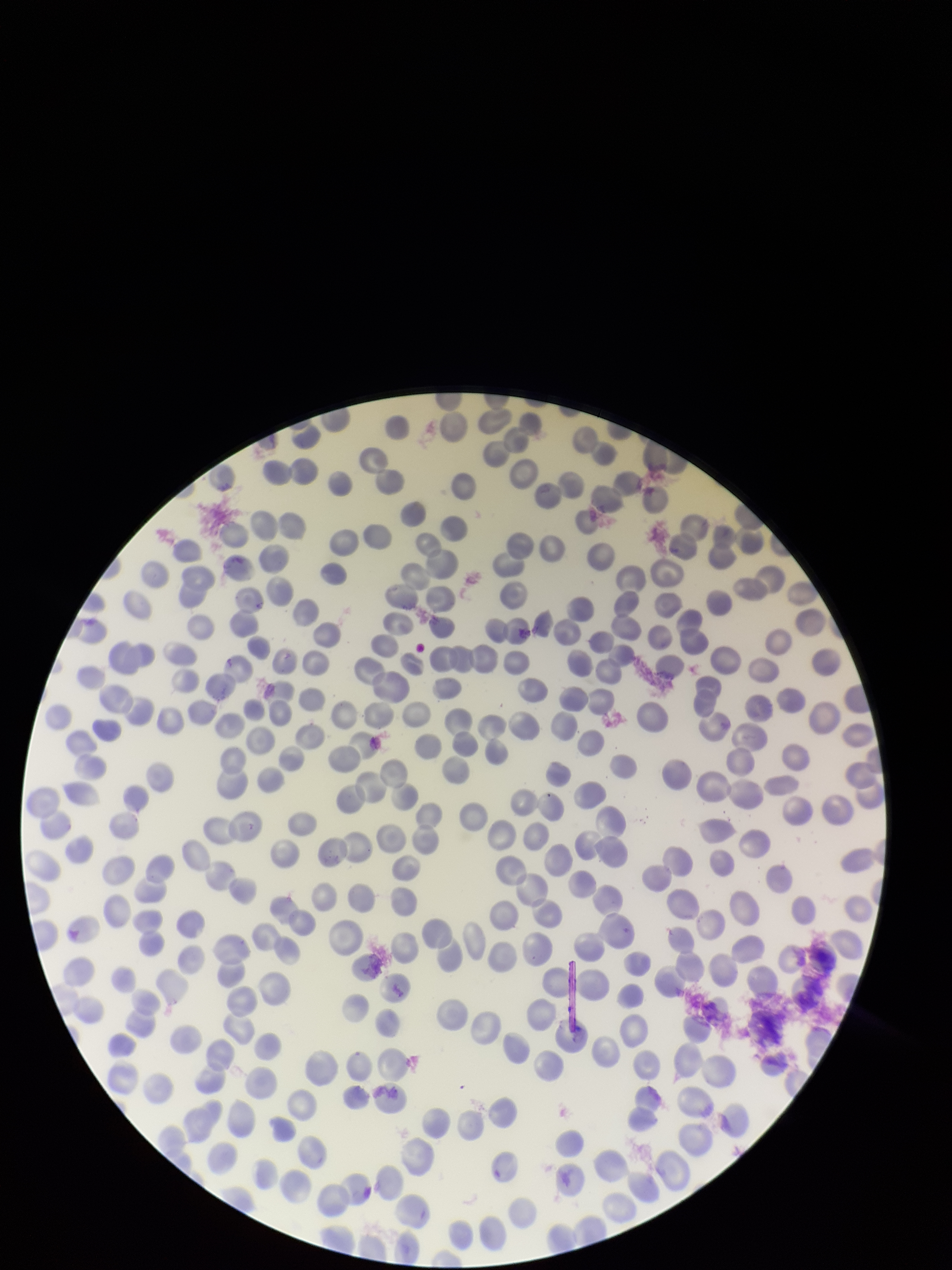

red blood cell count = 285
preparation = thin
image size = 952×1270 pixels
stain = Giemsa
field of view = one from this slide
capture = smartphone photograph through the microscope eyepiece
species reported for this patient = Plasmodium vivax
parasitized red blood cell count = 0
parasitized red blood cells = none identified
patient malaria status = infected